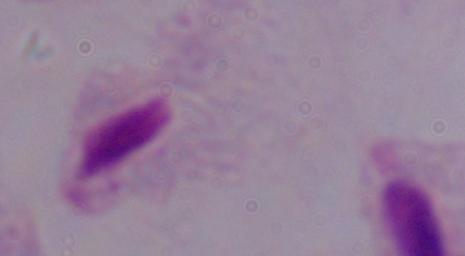

Photomicrograph. 1000x magnification. A trichomonad is seen.